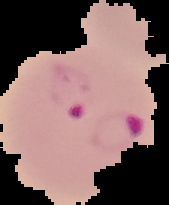

image size = 169×205 pixels
image type = segmented cell region on a black background
result = malaria parasites identified
preparation = thin blood film